Assess this cell for malaria.
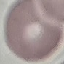

Uninfected.

Giemsa stain. Thin blood smear. Photographed with a smartphone camera at the microscope eyepiece. Cell patch, automatically extracted from a larger field of view and resized to 64 × 64 pixels.